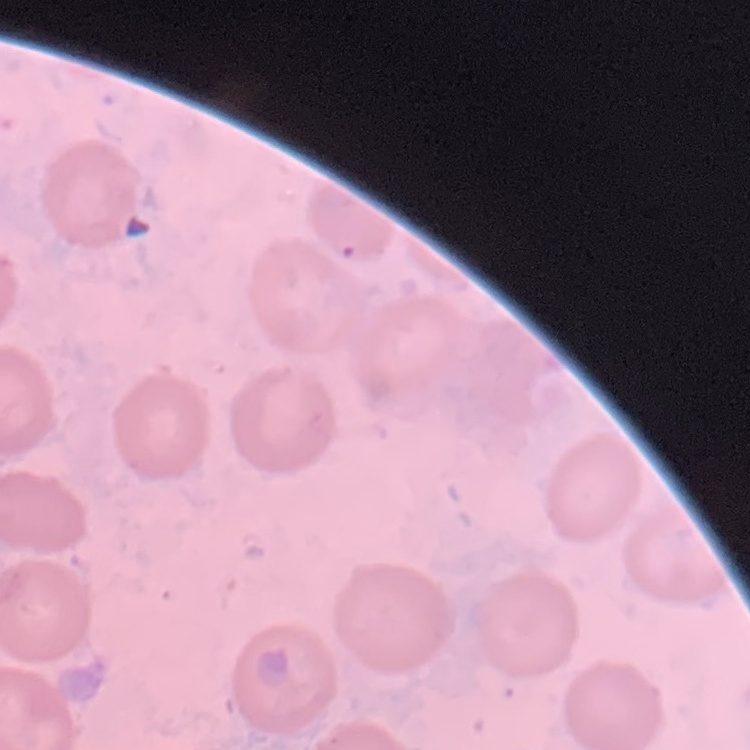

The red blood cells show no rouleaux formation. Thin peripheral smear. Field's or Giemsa stain. Square crop of a larger photomicrograph.